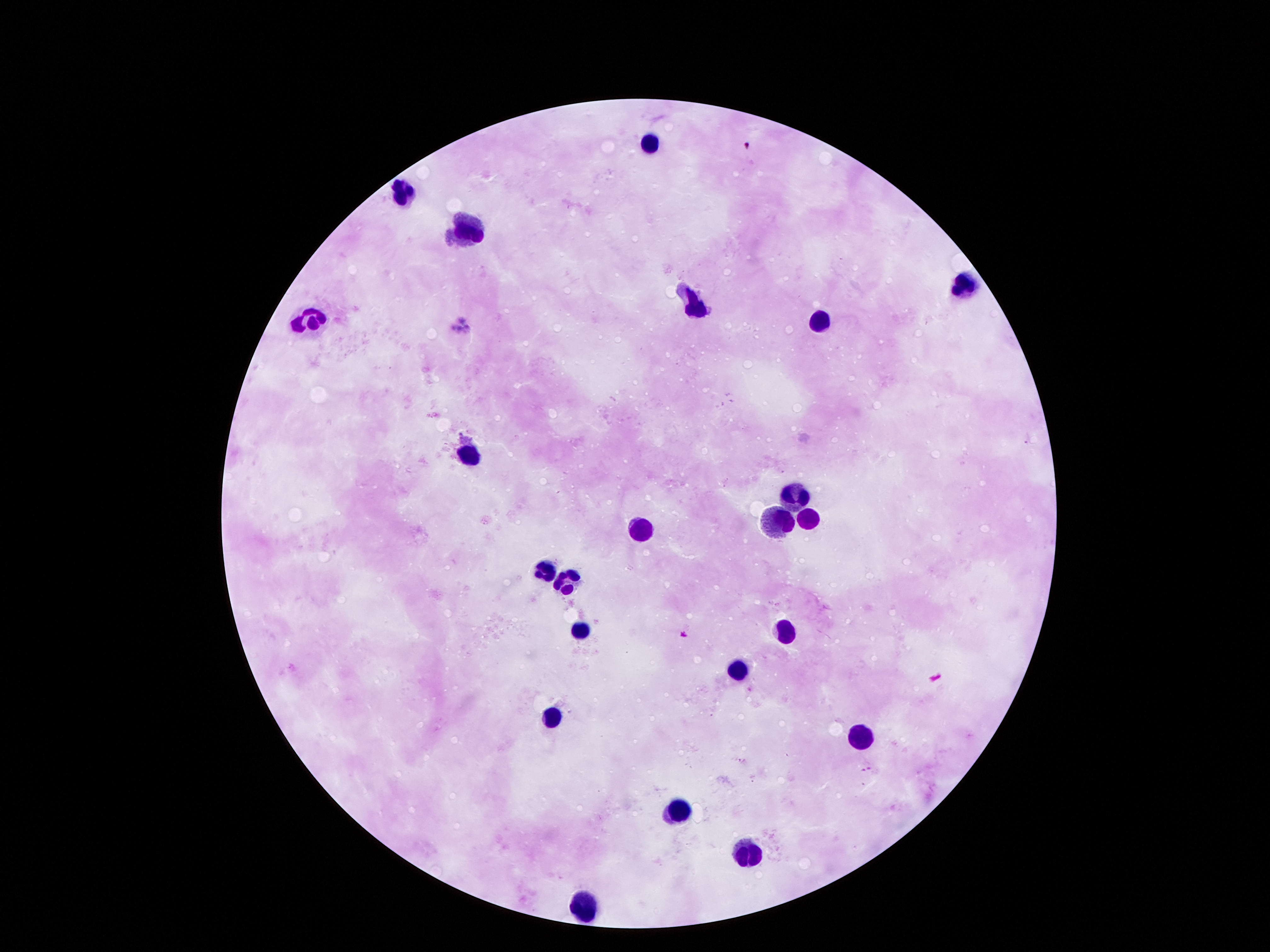
Approximate centers as [x, y] in pixels. Leukocyte locations: [649, 145], [401, 193], [469, 233], [964, 287], [697, 309], [310, 317], [822, 322], [467, 449], [791, 494], [803, 514], [774, 520], [639, 530], [539, 568], [567, 581], [784, 628], [581, 633], [738, 670], [550, 721], [860, 738], [673, 811], [748, 853], [589, 909]. 100x magnification. Giemsa-stained preparation. Image is 1270×952 pixels. Smartphone photograph taken through the microscope eyepiece. Patient malaria status: not infected. One field from this slide. Thick blood film.